Locate every blood parasite and identify its species.
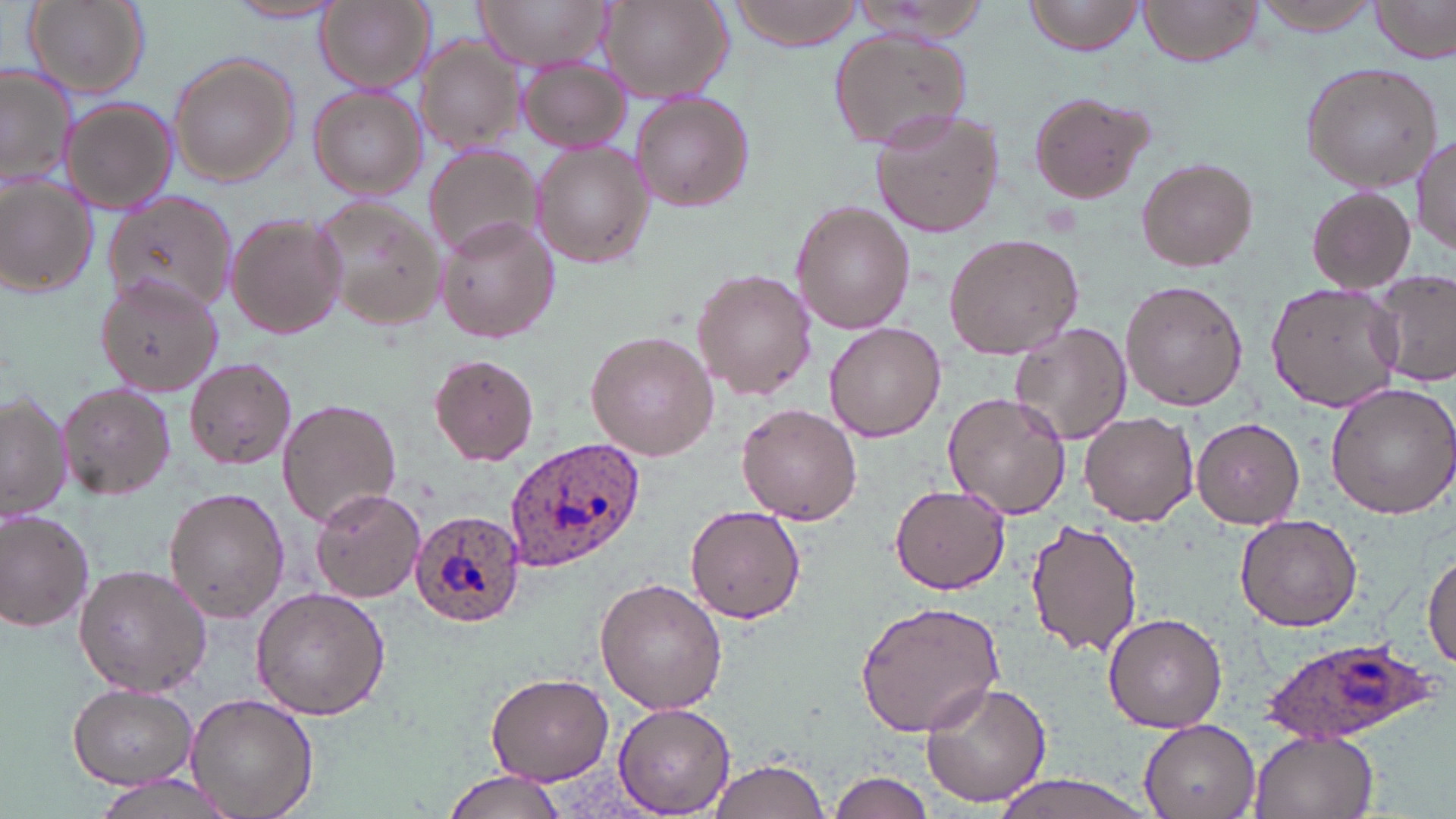
Approximate bounding boxes as named x1/y1/x2/y2 corners in pixels.
Plasmodium ovale-infected red blood cells: (x1=503, y1=436, x2=644, y2=573), (x1=410, y1=512, x2=526, y2=628), (x1=1261, y1=637, x2=1434, y2=745).
No Plasmodium falciparum, Plasmodium malariae, Plasmodium vivax, Babesia divergens, or Trypanosoma brucei observed.

Uninfected red blood cell locations: (x1=23, y1=0, x2=149, y2=98), (x1=473, y1=0, x2=610, y2=69), (x1=597, y1=0, x2=733, y2=103), (x1=723, y1=0, x2=868, y2=49), (x1=1025, y1=0, x2=1147, y2=55), (x1=1247, y1=0, x2=1392, y2=37), (x1=1372, y1=0, x2=1455, y2=64), (x1=315, y1=1, x2=432, y2=92), (x1=1138, y1=1, x2=1261, y2=67), (x1=226, y1=2, x2=343, y2=24), (x1=828, y1=28, x2=971, y2=152), (x1=413, y1=37, x2=526, y2=155), (x1=166, y1=52, x2=299, y2=187), (x1=516, y1=57, x2=628, y2=153), (x1=1301, y1=62, x2=1442, y2=191), (x1=1, y1=67, x2=77, y2=188), (x1=309, y1=85, x2=426, y2=201), (x1=629, y1=91, x2=754, y2=211), (x1=1026, y1=91, x2=1157, y2=207), (x1=59, y1=96, x2=177, y2=215), (x1=869, y1=108, x2=1001, y2=240), (x1=1412, y1=134, x2=1455, y2=255), (x1=531, y1=141, x2=655, y2=268), (x1=423, y1=145, x2=542, y2=260), (x1=1137, y1=157, x2=1258, y2=271), (x1=0, y1=176, x2=98, y2=299), (x1=1305, y1=186, x2=1417, y2=292), (x1=311, y1=193, x2=444, y2=333), (x1=105, y1=194, x2=240, y2=317), (x1=792, y1=201, x2=914, y2=335), (x1=224, y1=210, x2=350, y2=339), (x1=435, y1=216, x2=558, y2=344), (x1=943, y1=231, x2=1083, y2=360), (x1=1368, y1=269, x2=1456, y2=384), (x1=693, y1=270, x2=815, y2=398), (x1=95, y1=276, x2=223, y2=396), (x1=1121, y1=280, x2=1249, y2=410), (x1=1266, y1=282, x2=1403, y2=413), (x1=825, y1=322, x2=945, y2=440), (x1=1010, y1=322, x2=1132, y2=445), (x1=585, y1=331, x2=718, y2=460), (x1=428, y1=353, x2=539, y2=465), (x1=186, y1=359, x2=298, y2=471), (x1=56, y1=381, x2=176, y2=500), (x1=1324, y1=383, x2=1456, y2=519), (x1=0, y1=390, x2=71, y2=524), (x1=943, y1=391, x2=1071, y2=520), (x1=278, y1=397, x2=401, y2=528), (x1=738, y1=402, x2=863, y2=524), (x1=1079, y1=410, x2=1197, y2=528), (x1=1191, y1=416, x2=1305, y2=529), (x1=890, y1=485, x2=1009, y2=595), (x1=163, y1=487, x2=289, y2=622), (x1=309, y1=487, x2=426, y2=603), (x1=685, y1=504, x2=806, y2=623), (x1=0, y1=510, x2=98, y2=634), (x1=1233, y1=512, x2=1364, y2=631), (x1=1025, y1=517, x2=1144, y2=656), (x1=1424, y1=549, x2=1456, y2=670), (x1=72, y1=564, x2=212, y2=696), (x1=595, y1=578, x2=729, y2=717), (x1=251, y1=586, x2=392, y2=719), (x1=854, y1=599, x2=1004, y2=736), (x1=1104, y1=613, x2=1229, y2=733), (x1=485, y1=672, x2=615, y2=785), (x1=920, y1=680, x2=1054, y2=807), (x1=68, y1=684, x2=196, y2=786), (x1=186, y1=693, x2=318, y2=819), (x1=614, y1=703, x2=735, y2=815), (x1=1139, y1=719, x2=1261, y2=819), (x1=1251, y1=732, x2=1378, y2=819), (x1=704, y1=755, x2=835, y2=819), (x1=826, y1=769, x2=939, y2=819), (x1=440, y1=771, x2=565, y2=819), (x1=90, y1=773, x2=240, y2=819), (x1=980, y1=774, x2=1165, y2=819). Slide-level diagnosis: Plasmodium ovale. May-Grünwald-Giemsa stain. Thin blood smear. Single field of view. Image is 1456×819 pixels. Light microscopy. Captured at 1000x magnification.